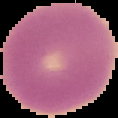
Summary:
  - Image size: 118×118 pixels
  - Image type: segmented cell region with the area outside set to black
  - Result: no Plasmodium parasites detected
  - Preparation: thin blood smear